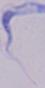

1000x magnification. Photomicrograph. A trypanosome is seen.